State which cell type is depicted.
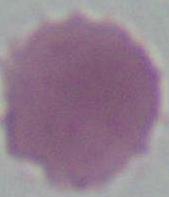
This is an erythrocyte.

Micrograph. 1000x magnification.